Classify this cell by malaria status.
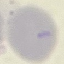
It is uninfected.

Acquired by smartphone through the microscope eyepiece. Automatically extracted cell patch, resized to 64 × 64 pixels. Thin blood smear. Giemsa-stained preparation.